Point out each Plasmodium parasite.
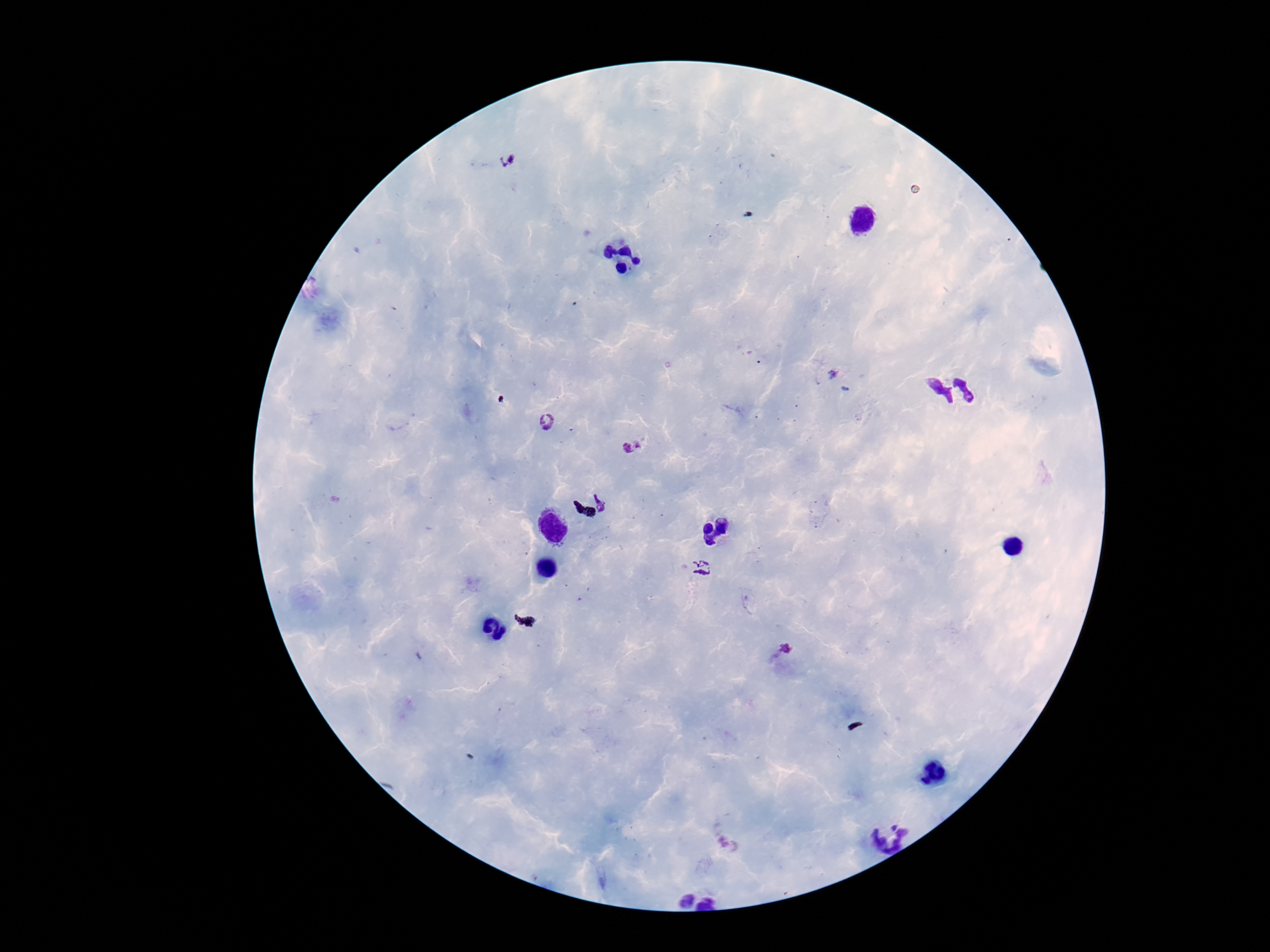
Approximate object centers, in pixels from the top-left corner.
Plasmodium parasites: (x=508, y=161), (x=548, y=423), (x=632, y=447), (x=606, y=499), (x=704, y=570), (x=786, y=647).

100x magnification. Photographed through the microscope eyepiece with a smartphone camera. Giemsa stain. Thick blood film. Image is 1270×952 pixels. One field from this slide. Patient malaria status: positive.